Classify this cell by malaria status.
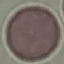
Uninfected.

{
  "image_type": "automatically extracted cell patch, resized to 64 × 64 pixels",
  "stain": "Giemsa",
  "capture": "smartphone camera at the microscope eyepiece",
  "preparation": "thin blood smear"
}